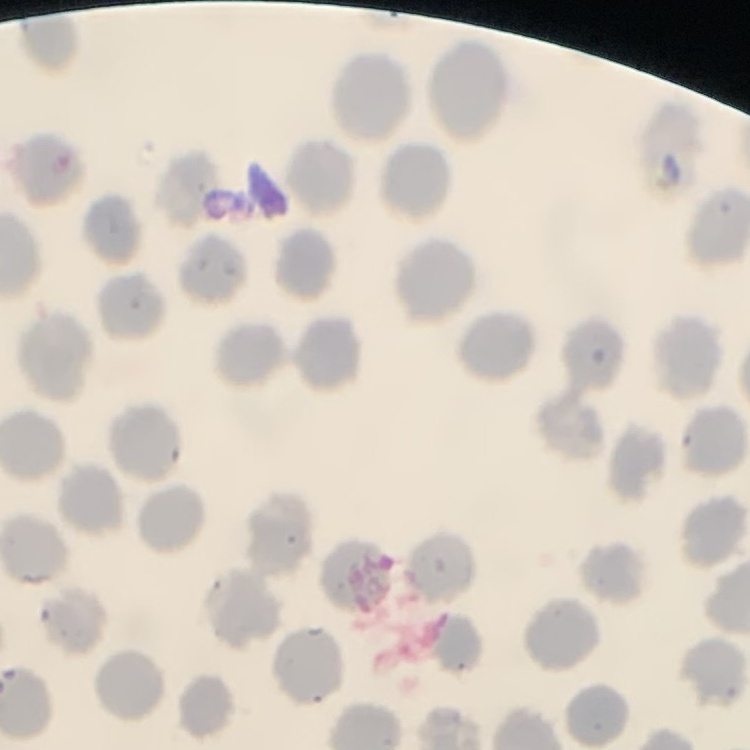
Summary:
  - Erythrocyte morphology: no rouleaux formation
  - Image type: square crop of a larger photomicrograph
  - Preparation: thin blood film
  - Stain: Field's or Giemsa